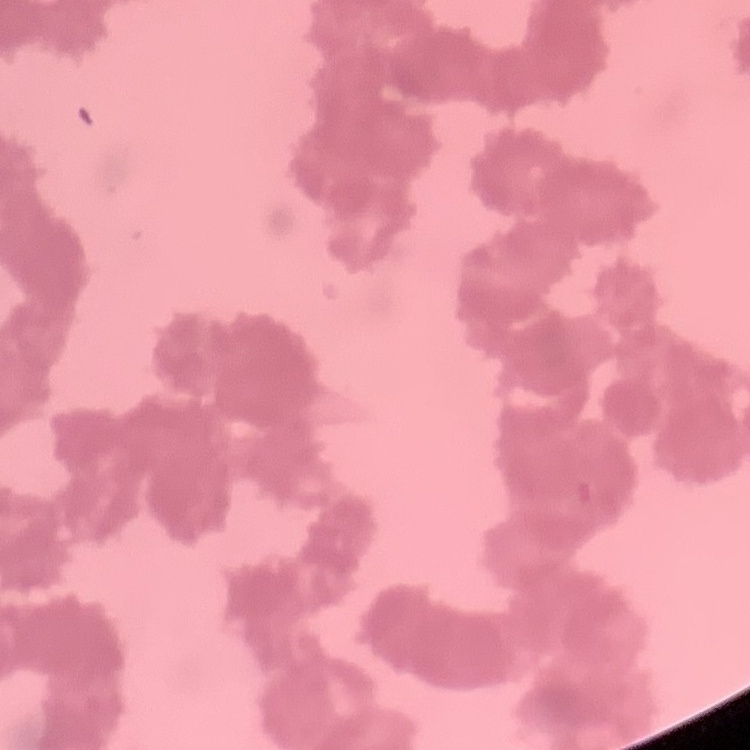

The erythrocytes show rouleaux formation. Thin blood smear. One tile cut from a larger photomicrograph. Field's or Giemsa stain.